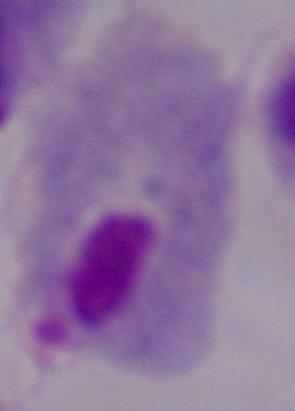

Captured at 1000x magnification. A trichomonad is shown. Photomicrograph.